Give the position of each P. falciparum parasite with its life-cycle stage, each leukocyte, and any debris.
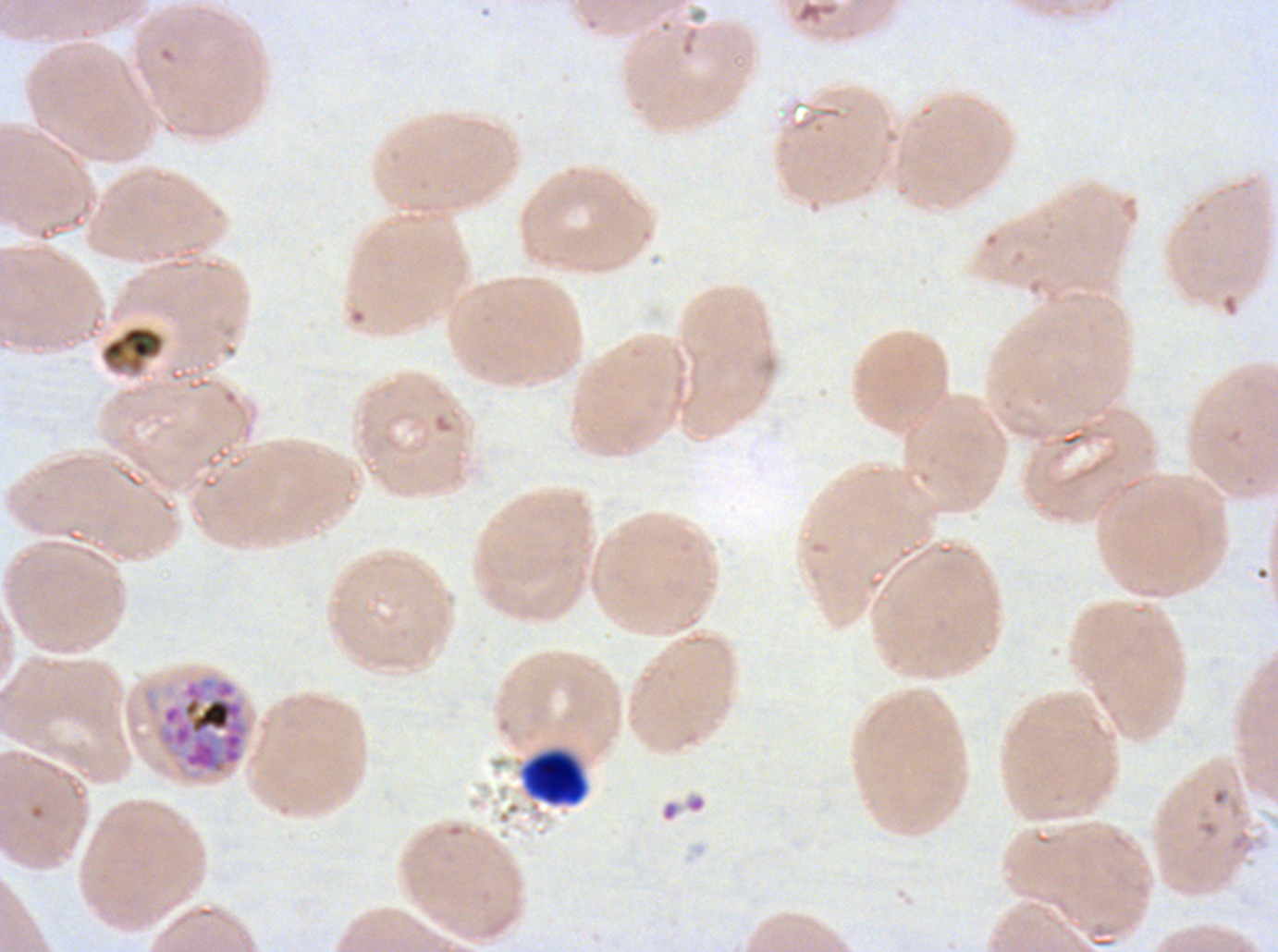

Approximate bounding boxes as {x1, y1, x2, y2} in pixels.
Late schizonts: {154, 676, 250, 775}.
Debris: {100, 324, 165, 375}, {521, 749, 588, 806}.
No rings, late-ring/early-trophozoite forms, mid trophozoites, late trophozoites, early schizonts, segmenters, gametocytes, or leukocytes observed.

preparation = thin blood smear
stain = Giemsa
image size = 1278×952 pixels
field of view = sub-image separated from a larger composite
specimen = ex-vivo P. falciparum culture from a patient in The Gambia, grown for 24 to 48 hours